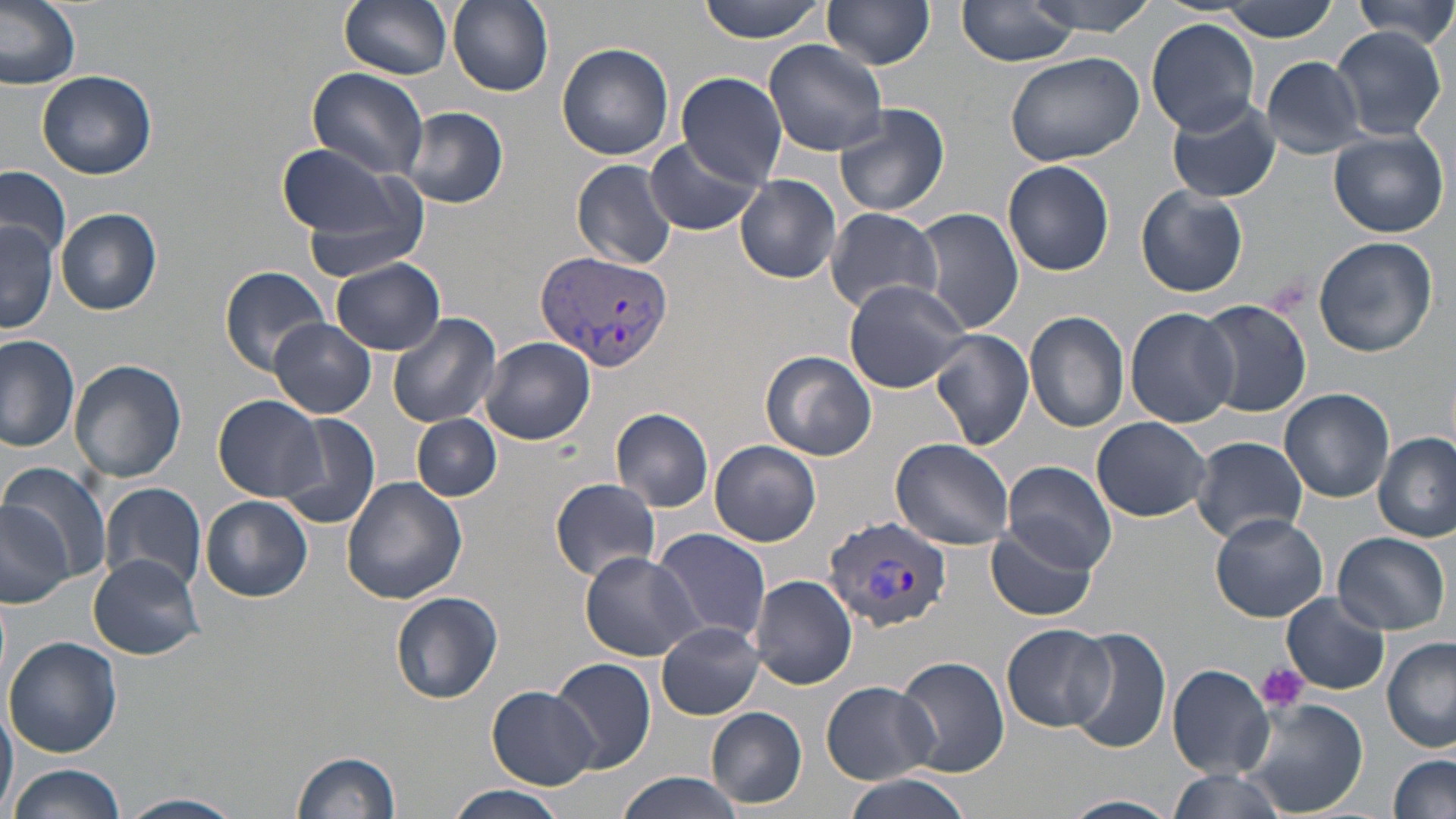

Approximate bounding boxes as [x1, y1, x2, y2] in pixels. Uninfected red blood cell locations: [0, 0, 80, 91], [337, 0, 453, 79], [448, 0, 554, 95], [695, 0, 827, 42], [1029, 0, 1159, 35], [1348, 0, 1456, 45], [821, 1, 938, 70], [1221, 1, 1341, 41], [955, 2, 1083, 68], [1145, 19, 1260, 134], [1330, 26, 1447, 139], [766, 36, 892, 156], [557, 42, 675, 161], [1005, 51, 1143, 167], [1260, 56, 1366, 159], [304, 67, 431, 180], [38, 69, 157, 180], [678, 71, 789, 188], [1167, 96, 1284, 203], [835, 103, 950, 218], [403, 107, 507, 208], [1328, 129, 1449, 237], [644, 137, 762, 238], [278, 143, 427, 265], [571, 158, 679, 270], [1002, 160, 1115, 276], [0, 166, 72, 260], [736, 174, 842, 283], [1136, 185, 1248, 297], [914, 207, 1024, 334], [56, 208, 164, 315], [824, 208, 943, 314], [1, 217, 57, 334], [1311, 236, 1438, 358], [333, 259, 445, 354], [220, 265, 331, 376], [842, 279, 970, 392], [1197, 299, 1313, 419], [1126, 307, 1243, 428], [1025, 312, 1131, 432], [386, 314, 501, 429], [270, 318, 374, 419], [930, 328, 1035, 451], [0, 335, 80, 451], [480, 337, 596, 445], [760, 350, 877, 461], [69, 358, 187, 482], [1280, 388, 1395, 503], [215, 396, 330, 502], [611, 407, 716, 511], [274, 414, 383, 531], [413, 414, 500, 500], [1092, 416, 1212, 523], [1374, 433, 1455, 543], [1188, 435, 1309, 543], [890, 436, 1018, 550], [709, 439, 821, 547], [1001, 461, 1117, 573], [4, 464, 113, 591], [342, 477, 468, 605], [551, 477, 661, 581], [98, 481, 209, 595], [202, 497, 313, 602], [0, 501, 74, 608], [1211, 512, 1328, 622], [988, 521, 1099, 622], [653, 528, 770, 647], [1332, 531, 1450, 635], [580, 550, 700, 661], [89, 555, 204, 659], [751, 575, 858, 690], [390, 592, 502, 705], [1282, 592, 1388, 695], [658, 622, 764, 720], [1003, 624, 1114, 731], [1065, 627, 1171, 756], [4, 636, 123, 759], [1381, 637, 1455, 751], [550, 656, 656, 774], [895, 656, 1010, 777], [1168, 664, 1274, 777], [821, 680, 940, 784], [487, 686, 598, 788], [0, 698, 17, 818], [1235, 698, 1368, 817], [706, 707, 807, 810], [293, 750, 401, 819], [1388, 755, 1456, 819], [6, 765, 126, 819], [1167, 769, 1284, 819], [614, 772, 745, 819], [841, 776, 972, 819], [442, 786, 571, 819], [121, 793, 243, 819], [1061, 795, 1180, 818]. Plasmodium vivax-infected red blood cell locations: [537, 251, 676, 372], [823, 514, 951, 630]. Platelet locations: [1256, 662, 1308, 712]. Slide-level diagnosis: Plasmodium vivax. 1000x magnification. May-Grünwald-Giemsa stain. Thin blood film. Image is 1456×819 pixels. Light microscopy. Single field of view.